Name the blood parasite species.
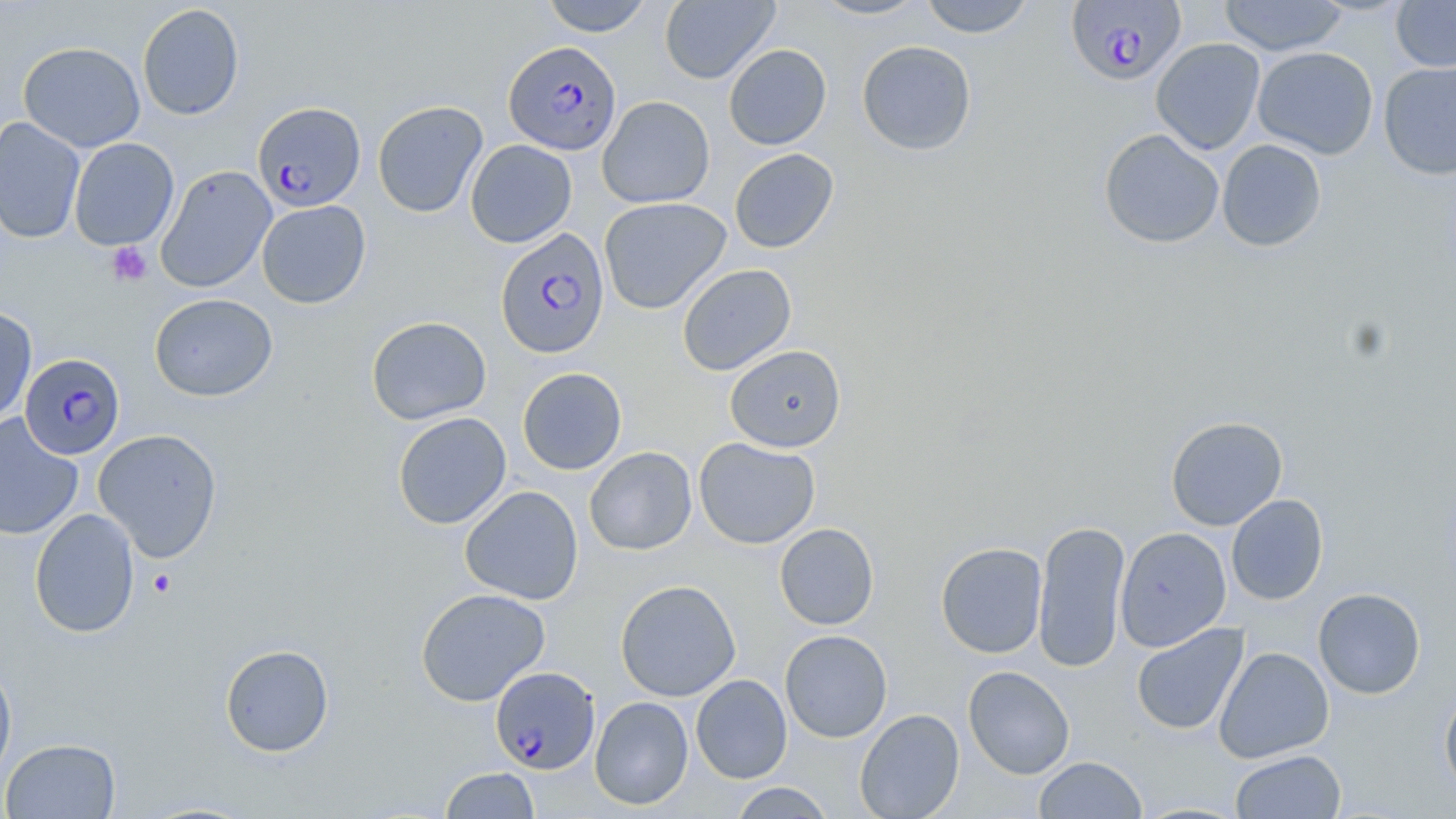

Plasmodium falciparum.

{
  "magnification": "1000x",
  "image_size": "1456×819 pixels",
  "uninfected_red_blood_cell_locations": "approximate bounding boxes as named x1/y1/x2/y2 corners in pixels: (x1=540, y1=0, x2=654, y2=36), (x1=659, y1=0, x2=780, y2=84), (x1=809, y1=0, x2=929, y2=20), (x1=919, y1=0, x2=1035, y2=38), (x1=1218, y1=0, x2=1348, y2=57), (x1=1391, y1=0, x2=1456, y2=72), (x1=137, y1=4, x2=244, y2=120), (x1=1151, y1=38, x2=1266, y2=155), (x1=857, y1=40, x2=977, y2=156), (x1=18, y1=41, x2=146, y2=152), (x1=723, y1=44, x2=832, y2=149), (x1=1252, y1=46, x2=1379, y2=160), (x1=1378, y1=61, x2=1456, y2=179), (x1=597, y1=95, x2=715, y2=208), (x1=372, y1=100, x2=488, y2=218), (x1=0, y1=115, x2=85, y2=244), (x1=1098, y1=128, x2=1225, y2=249), (x1=69, y1=137, x2=179, y2=251), (x1=1217, y1=139, x2=1327, y2=252), (x1=465, y1=140, x2=577, y2=248), (x1=729, y1=148, x2=839, y2=253), (x1=155, y1=165, x2=277, y2=293), (x1=599, y1=197, x2=731, y2=315), (x1=256, y1=200, x2=371, y2=309), (x1=677, y1=263, x2=797, y2=375), (x1=149, y1=293, x2=278, y2=401), (x1=0, y1=305, x2=37, y2=425), (x1=366, y1=316, x2=492, y2=425), (x1=725, y1=344, x2=846, y2=452), (x1=517, y1=367, x2=627, y2=475), (x1=392, y1=412, x2=511, y2=529), (x1=0, y1=414, x2=84, y2=541), (x1=1165, y1=415, x2=1288, y2=531), (x1=93, y1=428, x2=222, y2=562), (x1=694, y1=437, x2=820, y2=549), (x1=584, y1=447, x2=697, y2=555), (x1=459, y1=485, x2=584, y2=605), (x1=1226, y1=494, x2=1328, y2=605), (x1=29, y1=508, x2=140, y2=638), (x1=1033, y1=520, x2=1130, y2=673), (x1=775, y1=523, x2=878, y2=630), (x1=1115, y1=527, x2=1232, y2=652), (x1=935, y1=542, x2=1048, y2=659), (x1=615, y1=579, x2=741, y2=702), (x1=414, y1=588, x2=551, y2=706), (x1=1313, y1=588, x2=1426, y2=699), (x1=1131, y1=623, x2=1248, y2=735), (x1=779, y1=630, x2=892, y2=743), (x1=219, y1=643, x2=334, y2=757), (x1=1213, y1=647, x2=1334, y2=763), (x1=0, y1=660, x2=17, y2=783), (x1=963, y1=666, x2=1075, y2=779), (x1=690, y1=675, x2=792, y2=784), (x1=1439, y1=685, x2=1456, y2=800), (x1=590, y1=696, x2=693, y2=810), (x1=854, y1=709, x2=964, y2=819), (x1=1, y1=738, x2=121, y2=819), (x1=1231, y1=750, x2=1346, y2=818), (x1=1033, y1=756, x2=1147, y2=819), (x1=440, y1=767, x2=539, y2=818), (x1=727, y1=782, x2=836, y2=818)",
  "stain": "May-Grünwald-Giemsa",
  "modality": "optical microscopy",
  "plasmodium_falciparum_infected_red_blood_cell_locations": "approximate bounding boxes as named x1/y1/x2/y2 corners in pixels: (x1=1067, y1=2, x2=1187, y2=86), (x1=503, y1=41, x2=621, y2=156), (x1=253, y1=102, x2=366, y2=212), (x1=495, y1=227, x2=609, y2=359), (x1=19, y1=352, x2=126, y2=461), (x1=490, y1=666, x2=600, y2=774)",
  "platelet_locations": "approximate bounding boxes as named x1/y1/x2/y2 corners in pixels: (x1=106, y1=241, x2=152, y2=287), (x1=147, y1=569, x2=177, y2=598)",
  "field_of_view": "single",
  "preparation": "thin blood smear"
}